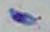

Toxoplasma gondii is shown. 1000x magnification. Micrograph.